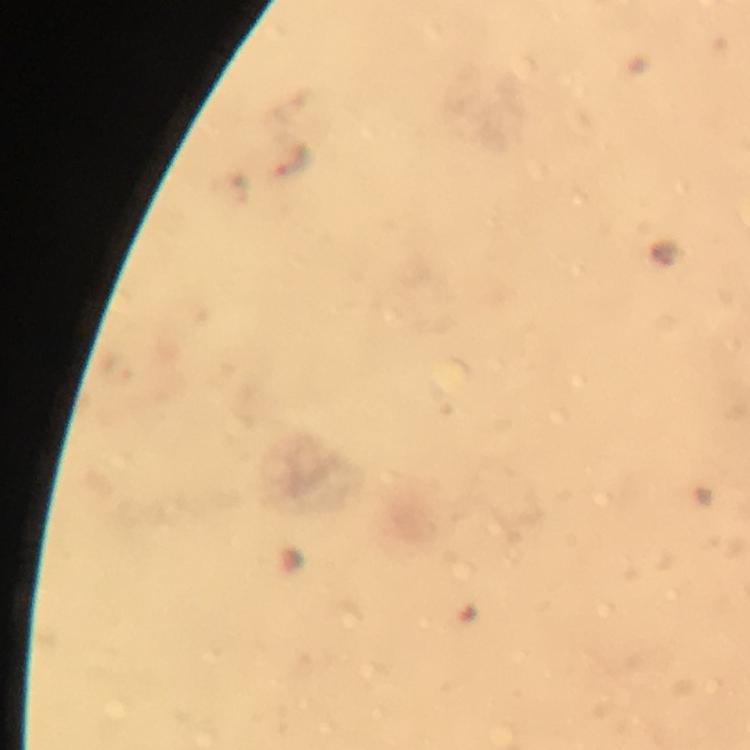

Approximate object centers, in pixels from the top-left corner. Malaria parasite locations: (x=293, y=157), (x=118, y=366). Image is 750×750 pixels. Giemsa stain. At 100x magnification. Photographed with a smartphone mounted on the microscope. Immersion oil was used. From a diagnostic examination for malaria. A crop from one field of view. Thick blood film.